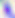
Summary:
  - Identification: Toxoplasma gondii
  - Magnification: 400x
  - Modality: photomicrograph